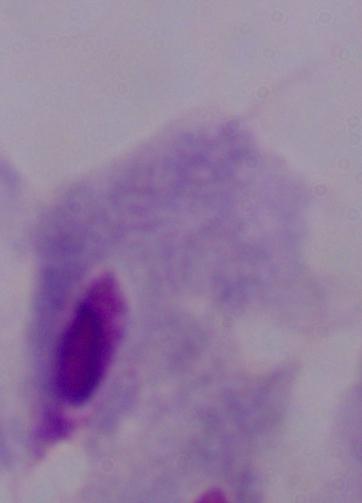

magnification = 1000x
modality = photomicrograph
identification = trichomonad